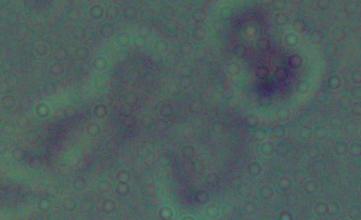 A Leishmania parasite is shown. Micrograph. Captured at 1000x magnification.